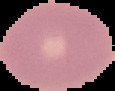

image type = segmented cell region on a black background
malaria status = uninfected
preparation = thin blood film
image size = 115×91 pixels